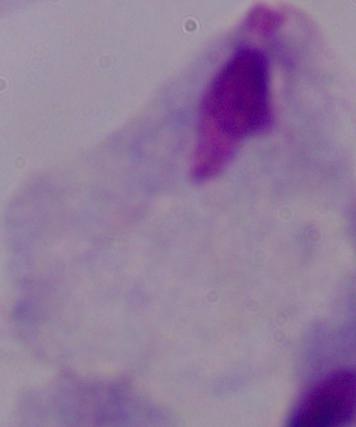 Captured at 1000x magnification. A trichomonad is seen. Photomicrograph.